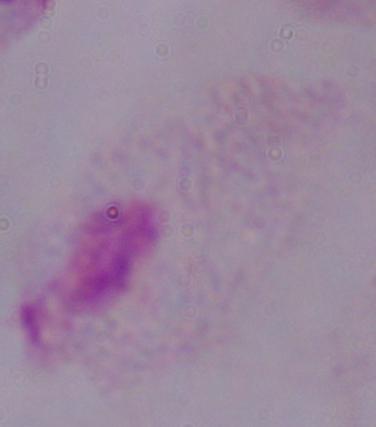

identification = trichomonad
modality = micrograph
magnification = 1000x